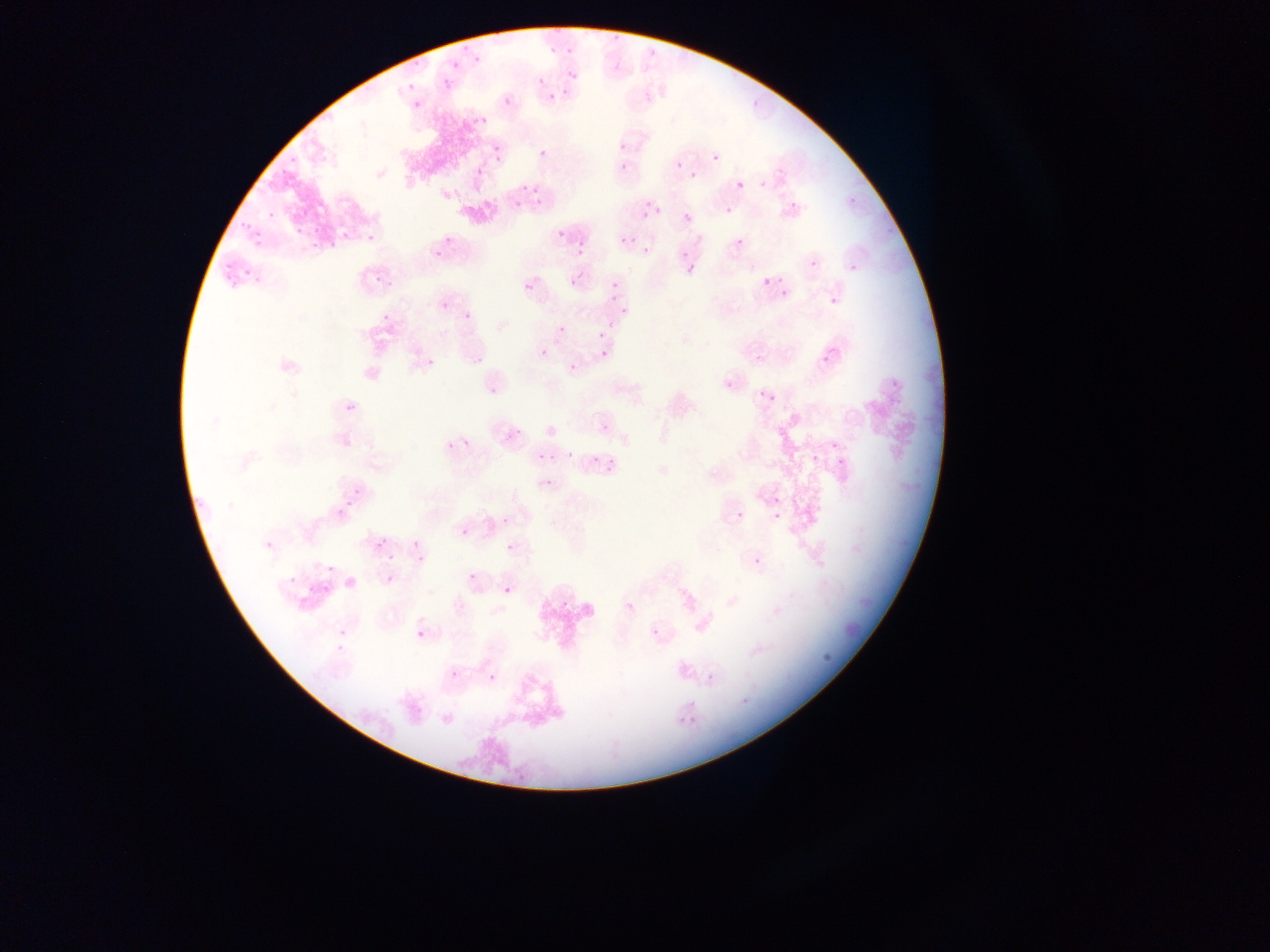

Approximate bounding boxes as [left, top, right, bottom] in pixels. Plasmodium parasite locations: [614, 33, 618, 43], [564, 45, 575, 57], [647, 46, 659, 56], [545, 48, 557, 56], [410, 54, 428, 73], [449, 58, 462, 67], [472, 58, 485, 66], [610, 60, 620, 75], [563, 66, 578, 79], [536, 73, 543, 83], [442, 75, 457, 91], [405, 81, 418, 94], [544, 87, 559, 98], [561, 87, 570, 99], [749, 94, 765, 113], [502, 95, 515, 109], [410, 97, 424, 112], [475, 117, 489, 128], [613, 139, 633, 151], [490, 144, 506, 164], [537, 146, 550, 160], [712, 152, 722, 163], [675, 160, 684, 169], [618, 161, 630, 174], [474, 166, 486, 179], [689, 171, 698, 181], [759, 177, 768, 191], [733, 180, 753, 190], [736, 180, 745, 190], [526, 183, 546, 198], [520, 185, 526, 194], [847, 195, 857, 204], [532, 198, 542, 207], [643, 201, 653, 211], [787, 202, 802, 212], [509, 204, 520, 214], [631, 205, 654, 221], [266, 206, 274, 218], [725, 207, 733, 216], [653, 210, 665, 217], [683, 212, 693, 223], [238, 218, 251, 232], [886, 218, 896, 230], [293, 224, 308, 239], [312, 224, 322, 237], [554, 227, 567, 241], [340, 228, 352, 243], [364, 229, 379, 245], [443, 232, 457, 248], [251, 233, 269, 252], [573, 234, 590, 249], [621, 236, 632, 246], [735, 237, 746, 249], [307, 243, 314, 253], [637, 244, 651, 254], [677, 244, 685, 259], [326, 245, 336, 252], [431, 247, 446, 262], [573, 249, 581, 258], [683, 256, 695, 275], [223, 257, 232, 268], [809, 258, 821, 270], [848, 262, 861, 275], [241, 265, 251, 278], [251, 267, 276, 283], [566, 269, 576, 287], [773, 270, 788, 285], [371, 273, 388, 290], [223, 276, 231, 285], [761, 277, 771, 288], [523, 281, 535, 294], [606, 281, 617, 292], [779, 286, 790, 296], [606, 293, 615, 304], [827, 295, 841, 310], [439, 299, 451, 311], [619, 300, 631, 317], [461, 307, 475, 320], [380, 313, 388, 321], [605, 321, 618, 333], [557, 325, 566, 335], [597, 330, 607, 340], [540, 348, 549, 358], [819, 348, 839, 370], [599, 349, 610, 361], [754, 352, 767, 367], [472, 354, 486, 368], [420, 356, 433, 367], [568, 363, 577, 372], [722, 378, 738, 395], [890, 379, 900, 387], [487, 384, 502, 399], [756, 391, 766, 397], [766, 393, 776, 405], [348, 400, 361, 417], [345, 402, 357, 414], [599, 422, 611, 434], [515, 424, 523, 435], [460, 431, 475, 447], [444, 437, 453, 450], [831, 441, 837, 450], [565, 450, 575, 460], [538, 452, 547, 463], [810, 453, 820, 464], [608, 454, 618, 464], [586, 455, 600, 466], [601, 457, 612, 472], [835, 457, 845, 465], [542, 478, 554, 489], [352, 486, 364, 498], [770, 495, 782, 508], [344, 499, 354, 507], [332, 505, 342, 516], [735, 510, 746, 521], [772, 512, 782, 522], [501, 515, 511, 527], [460, 527, 471, 538], [407, 531, 420, 548], [375, 539, 387, 552], [505, 542, 517, 554], [387, 554, 395, 565], [415, 555, 425, 562], [751, 556, 764, 569], [326, 564, 336, 574], [467, 571, 480, 584], [286, 575, 299, 588], [385, 576, 397, 590], [501, 585, 514, 598], [558, 599, 571, 614], [623, 599, 637, 615], [649, 625, 663, 640], [336, 627, 351, 638], [415, 628, 427, 641], [335, 643, 348, 656], [822, 646, 832, 664], [446, 667, 462, 683], [487, 672, 499, 685], [706, 672, 716, 683], [739, 695, 751, 707], [515, 768, 525, 783] | approximate [x, y] pixel centers of objects too small to bound: [465, 48]. Photographed through a microscope with a mobile-phone camera. Image is 1270×952 pixels. Single field of view. Collected in Ghana. Thin blood smear.